Report the malaria status of this cell.
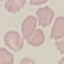

It is uninfected.

capture = smartphone through the microscope eyepiece
stain = Giemsa
preparation = thin blood smear
image type = automatically extracted cell patch, resized to 64 × 64 pixels